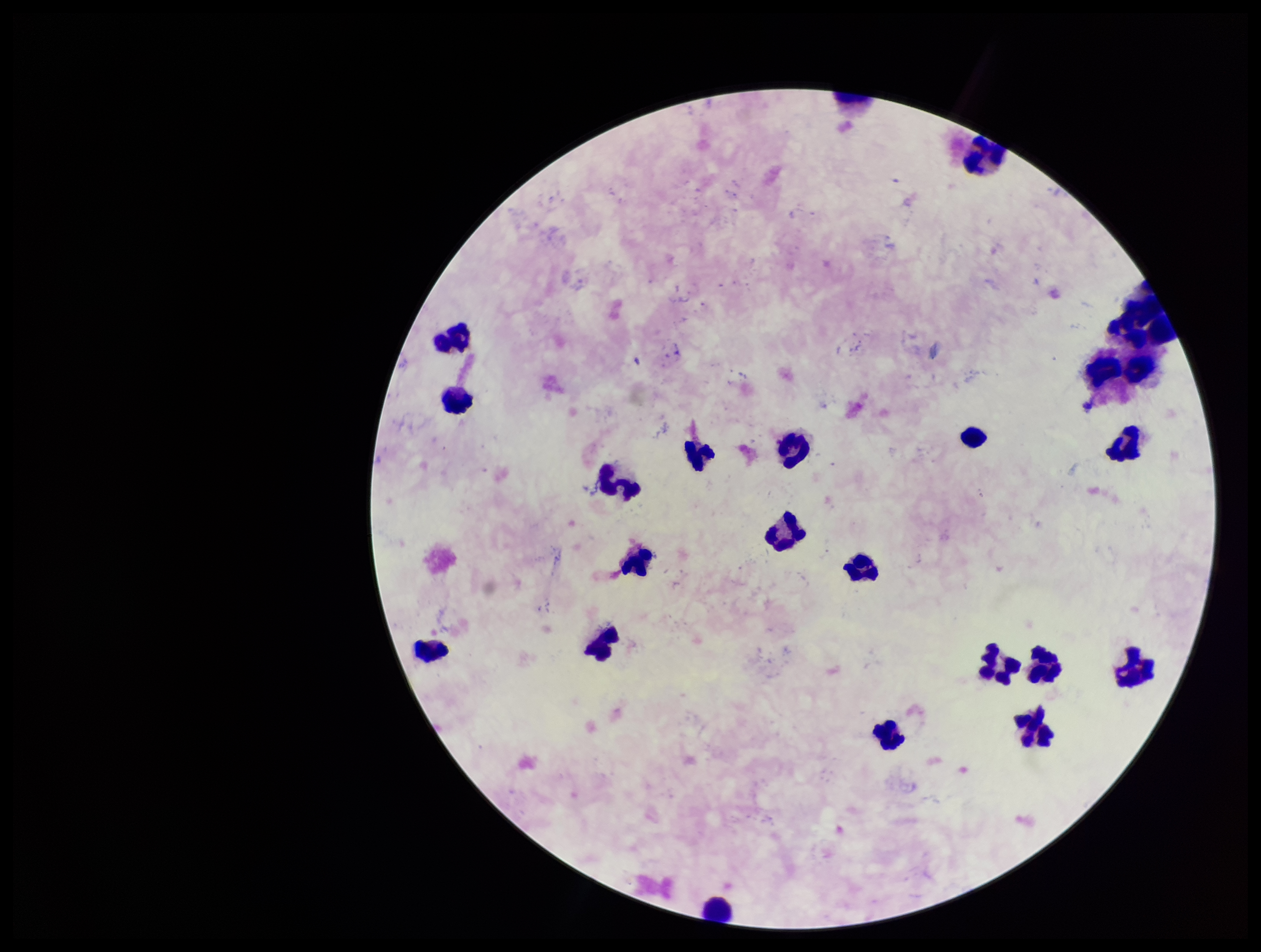
image_size: 1261×952 pixels
plasmodium_parasites: none seen
capture: smartphone photograph through the microscope eyepiece
leukocyte_count: 22
stain: Giemsa
parasite_count: 0
preparation: thick
patient_malaria_status: negative
field_of_view: one from this slide